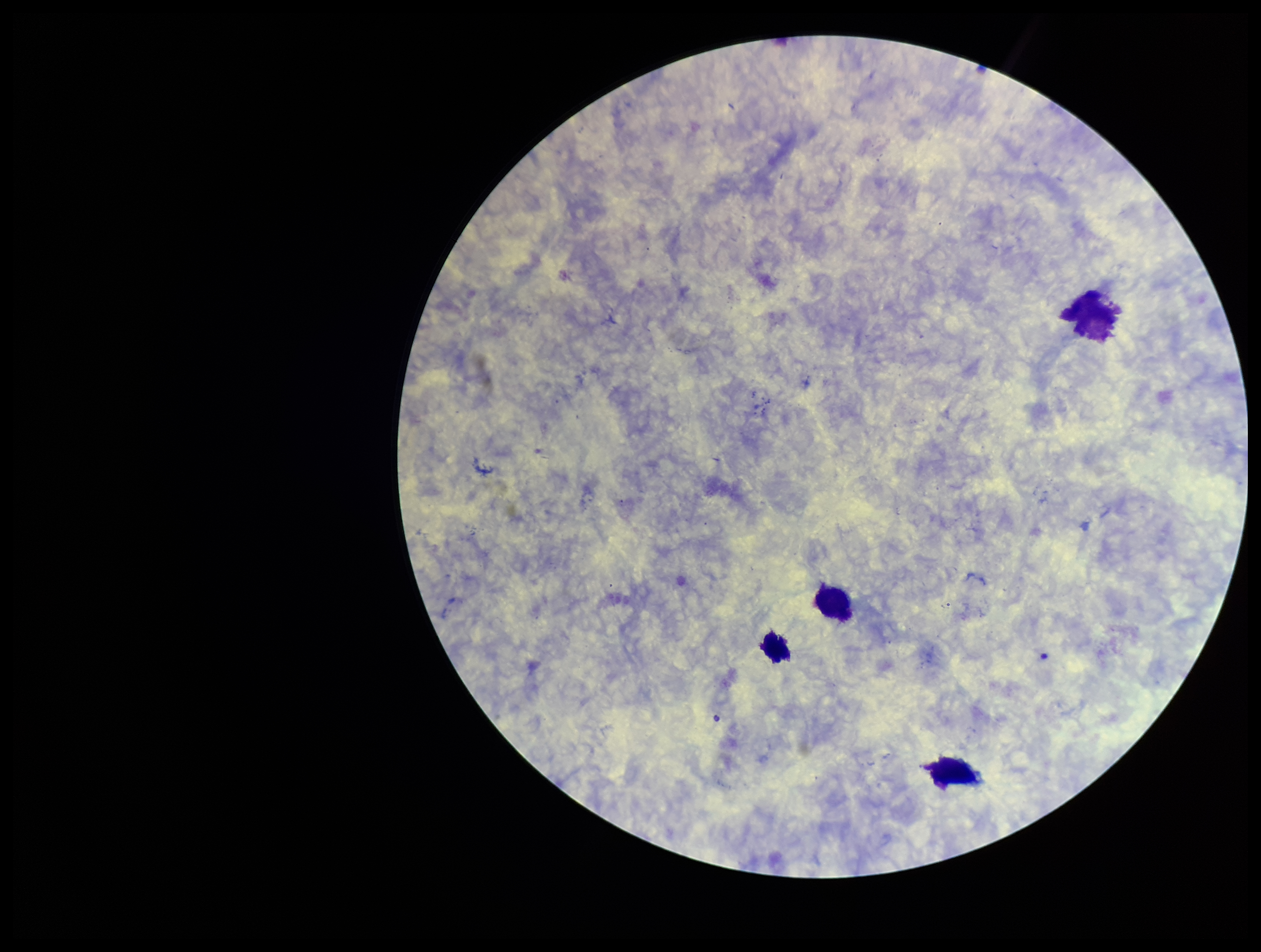

Giemsa stain. Single field of view. Smartphone photograph taken through the eyepiece of a microscope. Patient malaria status: negative. Leukocyte count: 4. Preparation: thick smear. Image is 1261×952 pixels. Plasmodium parasites: none detected. Parasite count: 0.